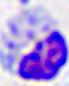
Summary:
  - Modality: photomicrograph
  - Magnification: 400x
  - Identification: leukocyte